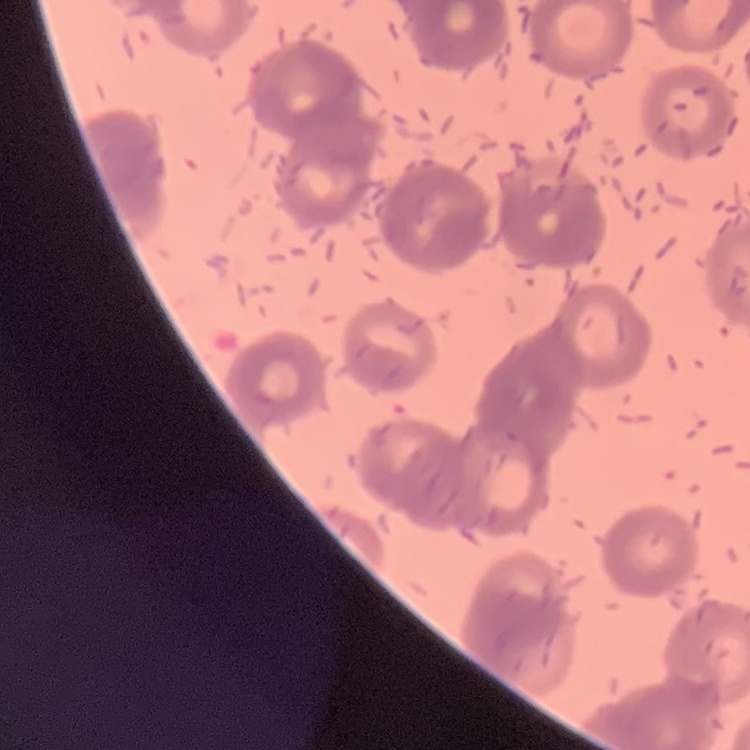 The red blood cells show rouleaux formation. Thin blood smear. Stained with either Field's or Giemsa. Square crop of a larger photomicrograph.